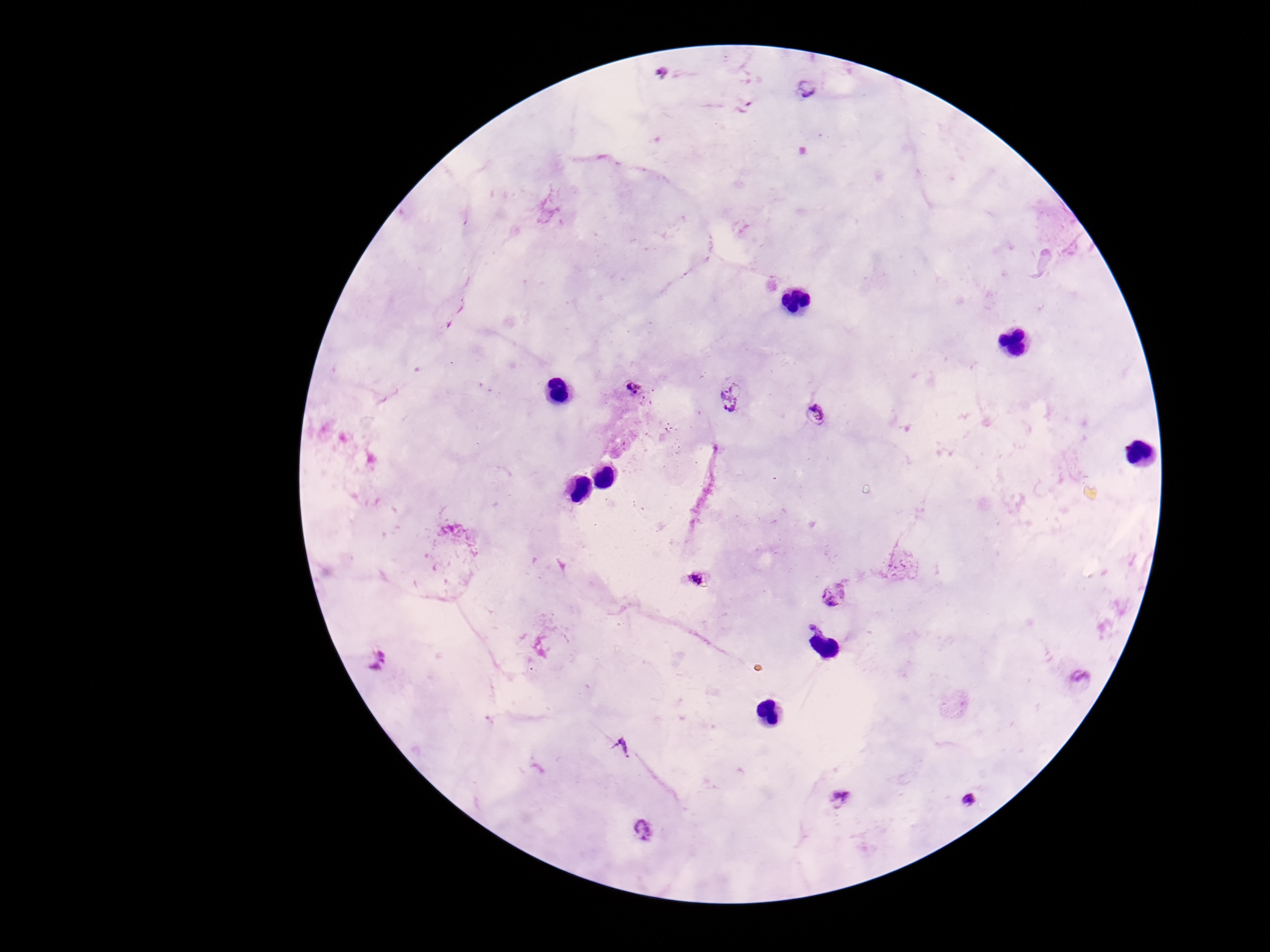
Approximate centers as (x, y) in pixels. Plasmodium parasite locations: (661, 72), (806, 88), (628, 390), (731, 394), (818, 414), (698, 581), (833, 594), (376, 660), (1081, 682), (621, 745), (842, 796), (968, 800), (643, 830). 100x magnification. Patient malaria status: positive. Giemsa stain. Image is 1270×952 pixels. One field from this slide. Photographed through the microscope eyepiece with a smartphone camera. Thick blood smear.